Identify the parasite.
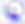

This is Toxoplasma gondii.

400x magnification. Micrograph.